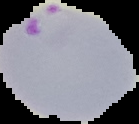

preparation = thin blood smear
image type = segmented cell region on a black background
image size = 139×124 pixels
malaria status = parasitized